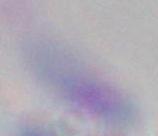
magnification = 1000x
identification = Toxoplasma gondii
modality = micrograph